Identify the cell.
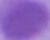

An erythrocyte.

magnification = 1000x
modality = photomicrograph